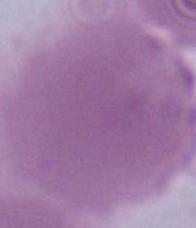
{
  "modality": "photomicrograph",
  "identification": "erythrocyte",
  "magnification": "1000x"
}